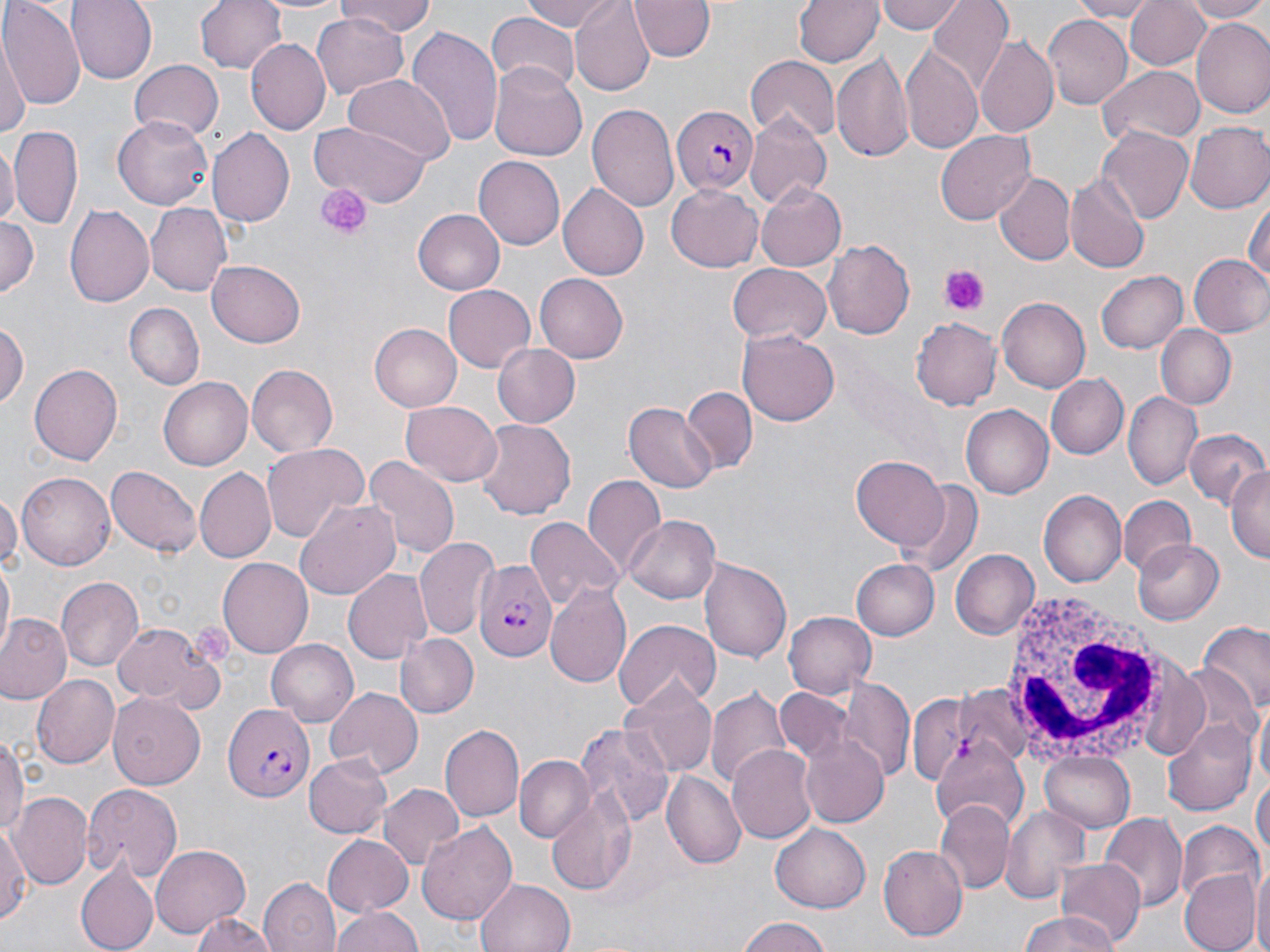

Approximate bounding boxes as named x1/y1/x2/y2 corners in pixels. Platelet locations: (x1=317, y1=183, x2=369, y2=239), (x1=939, y1=263, x2=988, y2=314). Uninfected red blood cell locations: (x1=69, y1=0, x2=155, y2=82), (x1=197, y1=0, x2=288, y2=74), (x1=335, y1=0, x2=436, y2=38), (x1=524, y1=0, x2=618, y2=33), (x1=570, y1=0, x2=655, y2=95), (x1=629, y1=0, x2=716, y2=61), (x1=794, y1=0, x2=883, y2=67), (x1=879, y1=0, x2=964, y2=35), (x1=930, y1=0, x2=1014, y2=89), (x1=1068, y1=0, x2=1157, y2=21), (x1=1125, y1=0, x2=1210, y2=70), (x1=1184, y1=0, x2=1270, y2=22), (x1=2, y1=1, x2=84, y2=113), (x1=312, y1=12, x2=408, y2=100), (x1=486, y1=14, x2=580, y2=94), (x1=1042, y1=14, x2=1132, y2=110), (x1=1192, y1=19, x2=1270, y2=115), (x1=406, y1=25, x2=504, y2=151), (x1=977, y1=36, x2=1061, y2=137), (x1=247, y1=39, x2=331, y2=134), (x1=0, y1=40, x2=27, y2=143), (x1=903, y1=45, x2=984, y2=156), (x1=831, y1=53, x2=913, y2=161), (x1=745, y1=56, x2=840, y2=140), (x1=129, y1=60, x2=223, y2=142), (x1=490, y1=63, x2=587, y2=161), (x1=1097, y1=67, x2=1203, y2=146), (x1=344, y1=76, x2=455, y2=162), (x1=587, y1=103, x2=678, y2=213), (x1=744, y1=112, x2=831, y2=207), (x1=112, y1=115, x2=215, y2=210), (x1=308, y1=120, x2=434, y2=207), (x1=1184, y1=122, x2=1270, y2=213), (x1=8, y1=125, x2=82, y2=231), (x1=207, y1=128, x2=295, y2=228), (x1=1099, y1=128, x2=1193, y2=222), (x1=935, y1=130, x2=1035, y2=225), (x1=0, y1=141, x2=16, y2=234), (x1=472, y1=156, x2=564, y2=250), (x1=1065, y1=169, x2=1150, y2=275), (x1=994, y1=171, x2=1074, y2=266), (x1=559, y1=183, x2=652, y2=280), (x1=667, y1=183, x2=765, y2=271), (x1=756, y1=183, x2=847, y2=272), (x1=1246, y1=191, x2=1269, y2=290), (x1=145, y1=202, x2=231, y2=297), (x1=65, y1=204, x2=154, y2=309), (x1=413, y1=210, x2=505, y2=296), (x1=0, y1=218, x2=39, y2=299), (x1=823, y1=240, x2=914, y2=340), (x1=1187, y1=253, x2=1270, y2=339), (x1=205, y1=262, x2=306, y2=348), (x1=727, y1=263, x2=833, y2=346), (x1=1096, y1=270, x2=1189, y2=354), (x1=536, y1=274, x2=628, y2=362), (x1=442, y1=286, x2=535, y2=372), (x1=996, y1=297, x2=1090, y2=392), (x1=124, y1=301, x2=204, y2=389), (x1=912, y1=318, x2=1001, y2=409), (x1=0, y1=321, x2=26, y2=407), (x1=370, y1=324, x2=461, y2=412), (x1=1156, y1=325, x2=1236, y2=410), (x1=738, y1=329, x2=838, y2=427), (x1=493, y1=342, x2=581, y2=427), (x1=246, y1=362, x2=339, y2=456), (x1=29, y1=364, x2=122, y2=465), (x1=1047, y1=375, x2=1127, y2=458), (x1=160, y1=377, x2=253, y2=470), (x1=680, y1=386, x2=757, y2=471), (x1=1125, y1=392, x2=1202, y2=491), (x1=400, y1=400, x2=503, y2=486), (x1=623, y1=403, x2=716, y2=492), (x1=961, y1=405, x2=1053, y2=499), (x1=474, y1=417, x2=574, y2=522), (x1=1185, y1=428, x2=1267, y2=510), (x1=261, y1=443, x2=367, y2=543), (x1=851, y1=456, x2=949, y2=548), (x1=362, y1=457, x2=458, y2=563), (x1=105, y1=464, x2=201, y2=561), (x1=1227, y1=466, x2=1270, y2=563), (x1=195, y1=469, x2=277, y2=561), (x1=16, y1=472, x2=116, y2=569), (x1=582, y1=474, x2=665, y2=577), (x1=901, y1=482, x2=983, y2=579), (x1=1039, y1=490, x2=1126, y2=587), (x1=0, y1=492, x2=19, y2=575), (x1=1118, y1=497, x2=1194, y2=577), (x1=293, y1=499, x2=400, y2=602), (x1=625, y1=515, x2=721, y2=604), (x1=526, y1=519, x2=623, y2=609), (x1=415, y1=537, x2=496, y2=640), (x1=1133, y1=537, x2=1225, y2=624), (x1=951, y1=549, x2=1038, y2=640), (x1=702, y1=556, x2=793, y2=661), (x1=217, y1=557, x2=314, y2=656), (x1=850, y1=557, x2=938, y2=639), (x1=1, y1=561, x2=14, y2=652), (x1=343, y1=568, x2=433, y2=664), (x1=57, y1=575, x2=143, y2=672), (x1=545, y1=584, x2=632, y2=687), (x1=784, y1=611, x2=875, y2=699), (x1=1, y1=615, x2=72, y2=705), (x1=615, y1=618, x2=720, y2=713), (x1=112, y1=620, x2=216, y2=711), (x1=1198, y1=625, x2=1270, y2=720), (x1=395, y1=633, x2=479, y2=719), (x1=265, y1=637, x2=359, y2=725), (x1=31, y1=675, x2=119, y2=769), (x1=839, y1=675, x2=912, y2=783), (x1=621, y1=677, x2=716, y2=776), (x1=927, y1=684, x2=1042, y2=781), (x1=708, y1=687, x2=792, y2=789), (x1=772, y1=687, x2=852, y2=770), (x1=324, y1=688, x2=423, y2=779), (x1=108, y1=692, x2=206, y2=789), (x1=1253, y1=699, x2=1269, y2=792), (x1=1163, y1=718, x2=1257, y2=814), (x1=440, y1=723, x2=524, y2=825), (x1=576, y1=724, x2=673, y2=829), (x1=0, y1=732, x2=26, y2=845), (x1=800, y1=732, x2=891, y2=830), (x1=934, y1=740, x2=1024, y2=833), (x1=727, y1=744, x2=817, y2=843), (x1=1039, y1=750, x2=1134, y2=833), (x1=305, y1=753, x2=392, y2=839), (x1=517, y1=757, x2=592, y2=843), (x1=1252, y1=765, x2=1269, y2=875), (x1=662, y1=771, x2=746, y2=870), (x1=81, y1=782, x2=184, y2=881), (x1=378, y1=785, x2=463, y2=870), (x1=545, y1=790, x2=639, y2=893), (x1=14, y1=791, x2=91, y2=888), (x1=935, y1=800, x2=1011, y2=893), (x1=999, y1=804, x2=1088, y2=904), (x1=1101, y1=813, x2=1185, y2=912), (x1=1177, y1=821, x2=1260, y2=905), (x1=417, y1=822, x2=516, y2=924), (x1=0, y1=823, x2=29, y2=927), (x1=770, y1=824, x2=870, y2=912), (x1=324, y1=834, x2=415, y2=916), (x1=151, y1=843, x2=252, y2=937), (x1=879, y1=846, x2=968, y2=942), (x1=1056, y1=860, x2=1145, y2=948), (x1=1250, y1=862, x2=1270, y2=952), (x1=76, y1=865, x2=158, y2=952), (x1=1180, y1=870, x2=1258, y2=952), (x1=259, y1=877, x2=340, y2=952), (x1=474, y1=877, x2=576, y2=952), (x1=331, y1=904, x2=424, y2=952), (x1=186, y1=910, x2=282, y2=952), (x1=1014, y1=911, x2=1125, y2=952), (x1=736, y1=917, x2=838, y2=952). Plasmodium falciparum-infected red blood cell locations: (x1=670, y1=107, x2=757, y2=194), (x1=472, y1=559, x2=558, y2=663), (x1=222, y1=705, x2=313, y2=799). White blood cell locations: (x1=998, y1=584, x2=1171, y2=760). Slide-level diagnosis: Plasmodium falciparum. Thin blood smear. Image is 1270×952 pixels. Light microscopy. Captured at 1000x magnification. Single field of view. May-Grünwald-Giemsa stain.